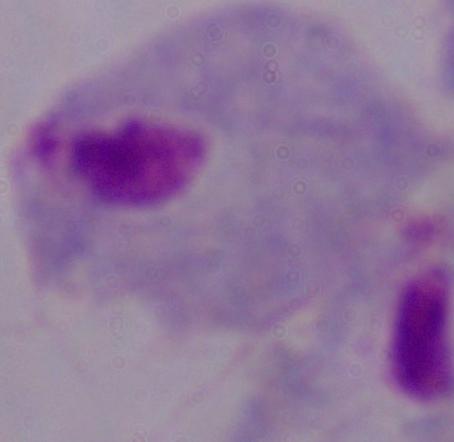
modality = photomicrograph
magnification = 1000x
identification = trichomonad